Classify this cell by malaria status.
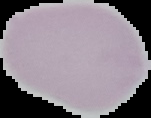
It is uninfected.

preparation = thin blood smear
image type = segmented cell region on a black background
image size = 151×118 pixels